Assess this cell for malaria.
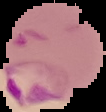

Parasitized.

Summary:
  - Image size: 106×112 pixels
  - Preparation: thin blood film
  - Image type: segmented cell region with the area outside set to black